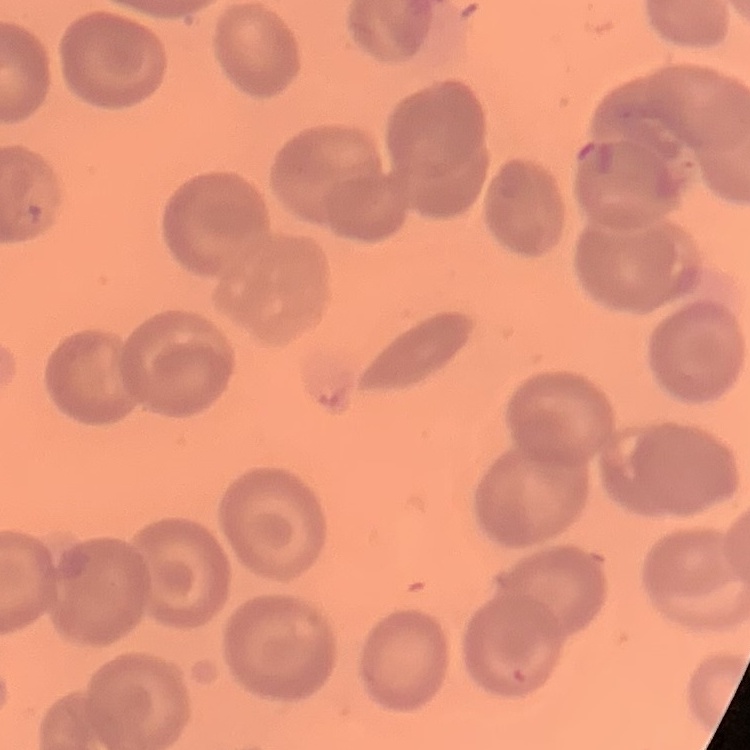 The erythrocytes exhibit no rouleaux formation. Stained with either Field's or Giemsa. Thin peripheral smear. One tile cut from a larger photomicrograph.